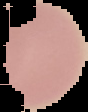
Summary:
  - Malaria status: uninfected
  - Preparation: thin blood smear
  - Image size: 88×112 pixels
  - Image type: cell region segmented out of the field of view; surrounding area masked to black